Assess this cell for malaria.
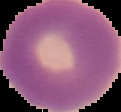

It is uninfected.

{
  "image_size": "121×112 pixels",
  "preparation": "thin blood film",
  "image_type": "cell region segmented out of the field of view; surrounding area masked to black"
}